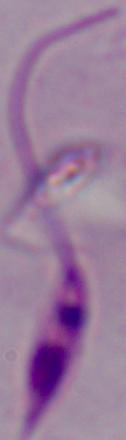

identification = Leishmania
magnification = 1000x
modality = photomicrograph